State which parasite is depicted.
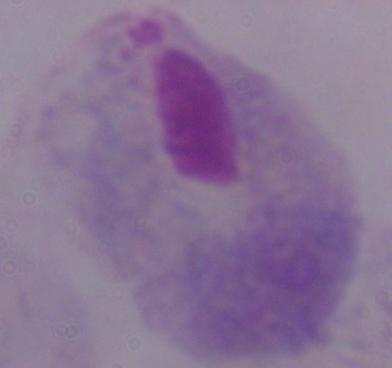

This is a trichomonad.

Micrograph. 1000x magnification.